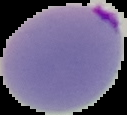
Image is 127×115 pixels. Result: malaria parasites detected. From a thin blood smear. The area outside the segmented cell region is set to black.